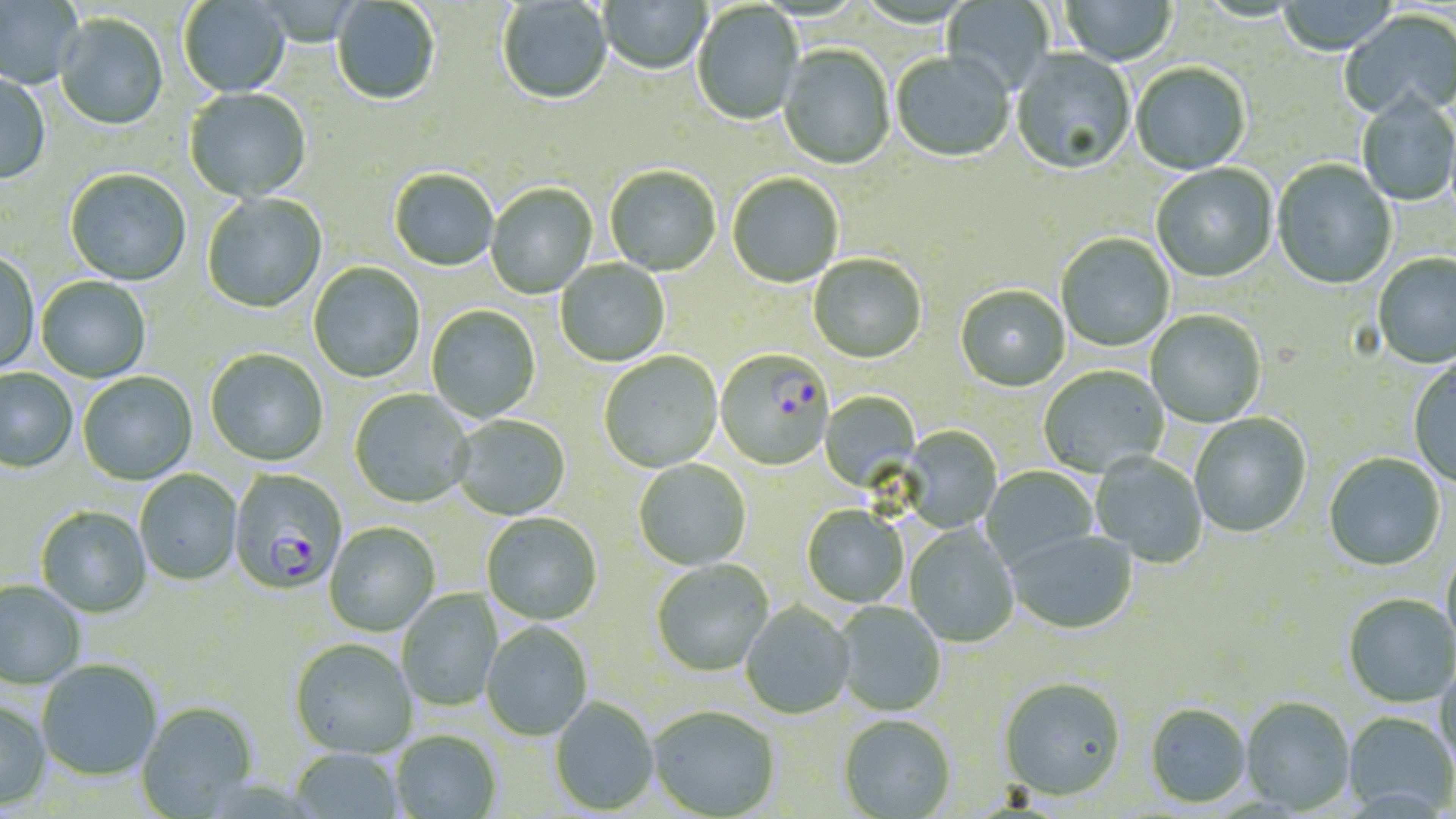
slide-level diagnosis = Plasmodium falciparum
field of view = one of a larger specimen
preparation = thin blood smear
stain = May-Grünwald-Giemsa
uninfected red blood cell locations = approximate bounding boxes as (x1, y1, x2, y2) in pixels: (0, 0, 83, 90), (179, 0, 291, 98), (599, 0, 711, 76), (942, 0, 1054, 96), (1061, 0, 1176, 67), (1277, 0, 1398, 57), (332, 1, 440, 107), (497, 1, 613, 107), (692, 3, 804, 126), (1339, 9, 1456, 122), (54, 15, 168, 131), (778, 46, 895, 171), (1010, 49, 1136, 177), (891, 53, 1014, 164), (1131, 64, 1250, 176), (0, 71, 51, 186), (184, 88, 312, 203), (1357, 93, 1456, 207), (1272, 161, 1397, 291), (1152, 164, 1278, 284), (605, 166, 721, 277), (64, 170, 191, 286), (389, 170, 499, 273), (727, 174, 844, 289), (486, 184, 597, 299), (202, 193, 328, 314), (1056, 234, 1175, 352), (0, 252, 40, 375), (1372, 254, 1456, 370), (808, 255, 926, 365), (555, 259, 670, 367), (308, 262, 425, 384), (37, 277, 151, 383), (955, 286, 1070, 393), (426, 305, 541, 423), (1146, 311, 1267, 427), (205, 350, 329, 468), (599, 352, 723, 474), (1409, 360, 1456, 489), (1039, 366, 1169, 477), (0, 369, 77, 473), (78, 373, 197, 486), (349, 389, 475, 509), (819, 391, 921, 493), (1189, 413, 1311, 539), (452, 416, 570, 521), (900, 426, 1002, 533), (1090, 453, 1207, 568), (1323, 453, 1445, 572), (634, 459, 751, 570), (981, 466, 1099, 569), (135, 470, 242, 586), (35, 506, 152, 618), (802, 506, 908, 608), (482, 513, 603, 626), (324, 523, 440, 636), (904, 525, 1019, 647), (1005, 530, 1139, 635), (1441, 546, 1456, 664), (651, 561, 775, 677), (0, 581, 86, 690), (396, 589, 503, 711), (1343, 595, 1455, 708), (741, 601, 855, 719), (834, 602, 947, 716), (481, 622, 593, 742), (289, 639, 417, 760), (36, 660, 163, 782), (1435, 663, 1456, 776), (998, 678, 1127, 805), (549, 697, 659, 815), (1241, 698, 1355, 815), (0, 700, 51, 810), (135, 702, 257, 818), (1145, 705, 1251, 809), (649, 708, 780, 818), (1343, 712, 1455, 818), (838, 717, 956, 818), (390, 731, 502, 819), (288, 748, 404, 818)
Plasmodium falciparum-infected red blood cell locations = approximate bounding boxes as (x1, y1, x2, y2) in pixels: (715, 351, 833, 471), (228, 470, 348, 597)
magnification = 1000x
image size = 1456×819 pixels
modality = light microscopy